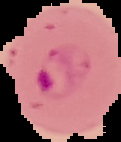

Image is 121×142 pixels. From a thin blood film. The area outside the segmented cell region is set to black. Malaria status: parasitized.